Report the malaria status of this cell.
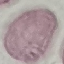
It is uninfected.

Acquired by smartphone through the microscope eyepiece. Automatically extracted cell patch, resized to 64 × 64 pixels. Giemsa-stained preparation. Thin blood film.